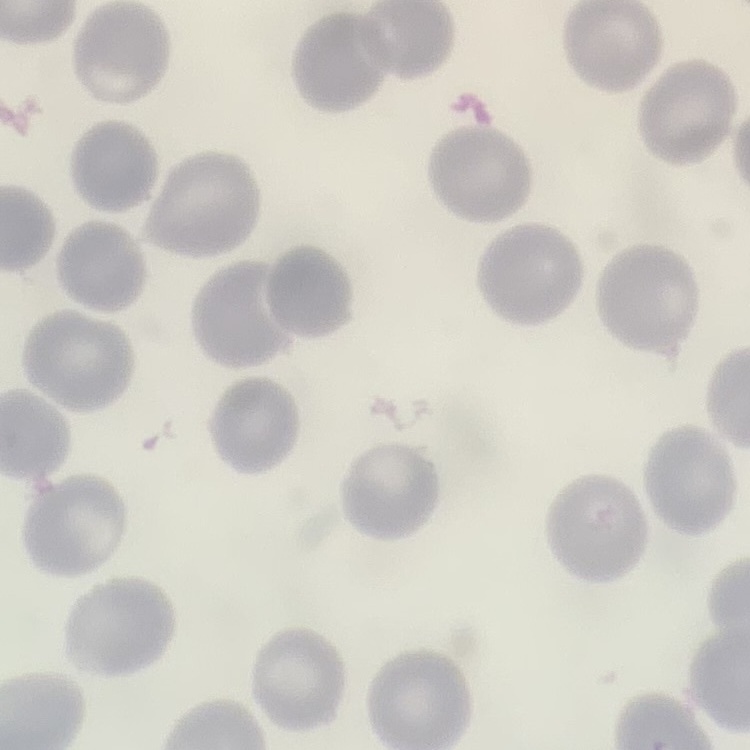
erythrocyte morphology = no rouleaux formation
preparation = thin blood film
stain = Field's or Giemsa
image type = square crop of a larger photomicrograph